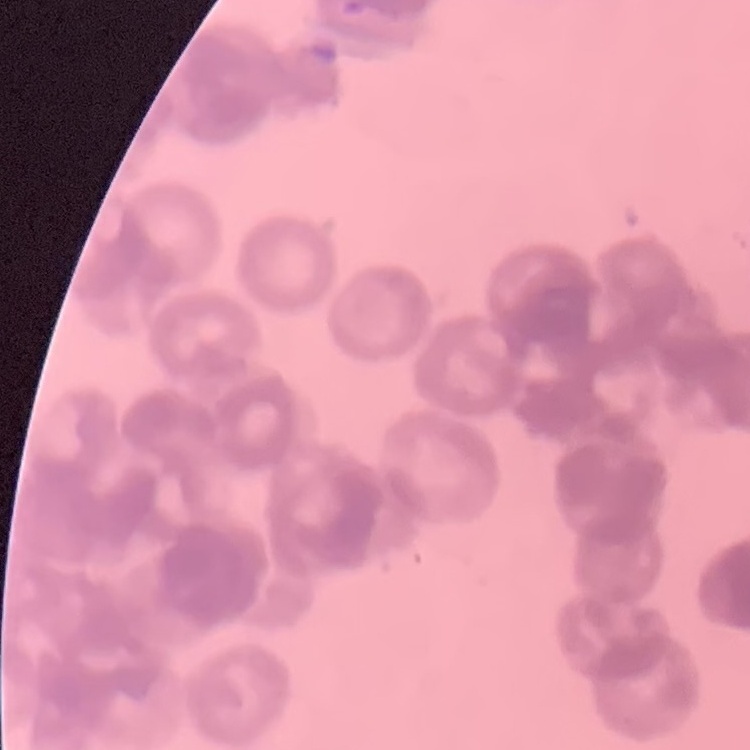
red blood cell morphology = rouleaux formation
preparation = thin peripheral smear
image type = one tile cut from a larger photomicrograph
stain = Field's or Giemsa